Give the extent of all Plasmodium falciparum-infected red blood cells.
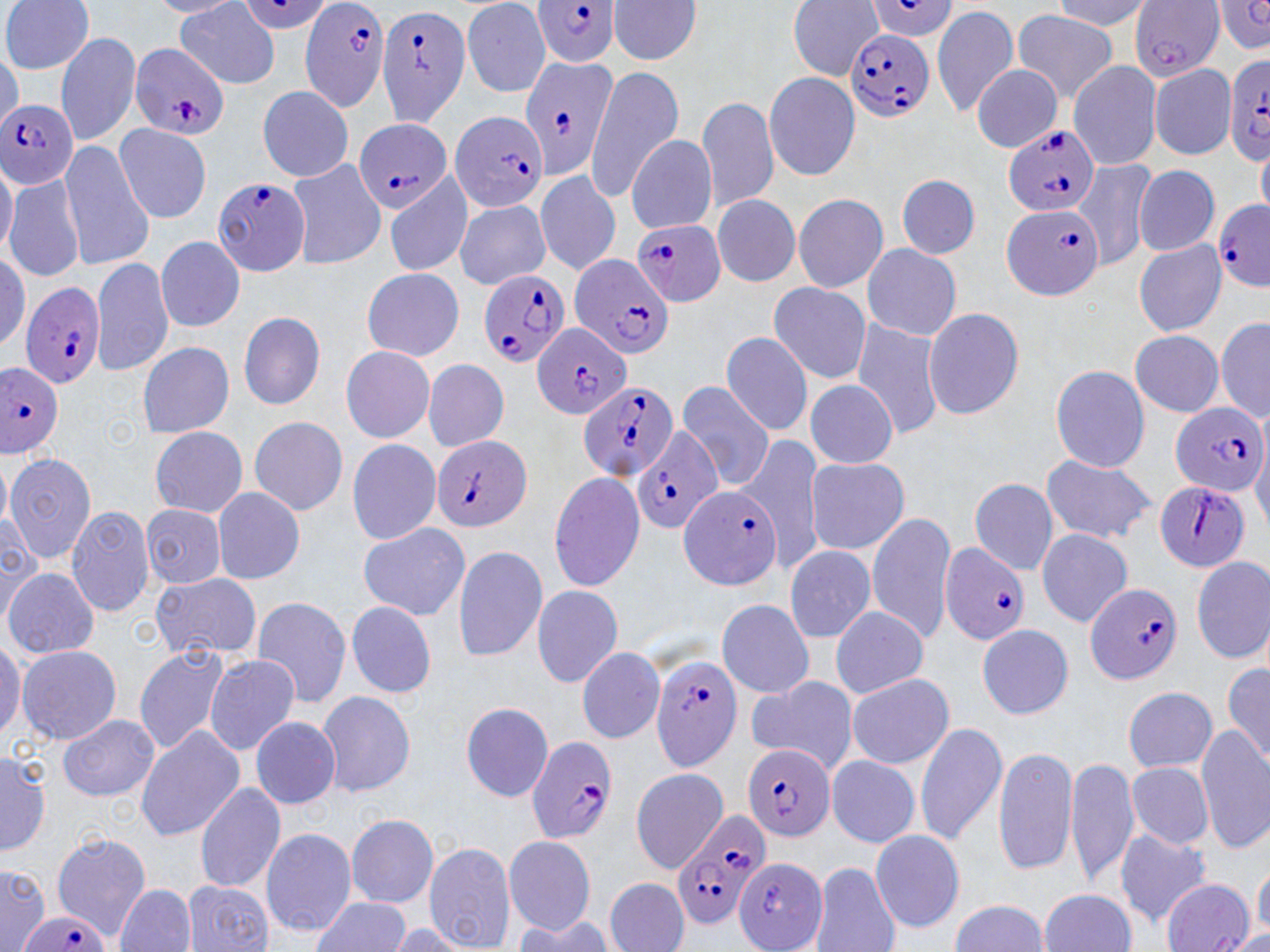

Approximate bounding boxes as named x1/y1/x2/y2 corners in pixels.
Plasmodium falciparum-infected red blood cells: (x1=533, y1=0, x2=622, y2=67), (x1=296, y1=5, x2=391, y2=110), (x1=380, y1=11, x2=466, y2=126), (x1=840, y1=26, x2=940, y2=122), (x1=134, y1=39, x2=226, y2=137), (x1=522, y1=55, x2=616, y2=182), (x1=1229, y1=56, x2=1270, y2=164), (x1=1, y1=99, x2=80, y2=191), (x1=350, y1=121, x2=454, y2=216), (x1=1006, y1=124, x2=1103, y2=213), (x1=211, y1=179, x2=307, y2=276), (x1=1209, y1=197, x2=1265, y2=293), (x1=1001, y1=202, x2=1101, y2=301), (x1=631, y1=220, x2=727, y2=307), (x1=567, y1=256, x2=673, y2=359), (x1=481, y1=271, x2=569, y2=373), (x1=21, y1=282, x2=103, y2=386), (x1=534, y1=324, x2=628, y2=419), (x1=0, y1=362, x2=64, y2=459), (x1=582, y1=388, x2=676, y2=478), (x1=1170, y1=401, x2=1268, y2=492), (x1=639, y1=429, x2=723, y2=538), (x1=428, y1=433, x2=532, y2=535), (x1=1150, y1=474, x2=1253, y2=570), (x1=680, y1=490, x2=780, y2=592), (x1=943, y1=541, x2=1024, y2=647), (x1=1083, y1=580, x2=1181, y2=684), (x1=644, y1=653, x2=745, y2=763), (x1=527, y1=738, x2=614, y2=838), (x1=744, y1=745, x2=833, y2=839), (x1=671, y1=808, x2=770, y2=928), (x1=16, y1=910, x2=112, y2=952).

Summary:
  - White blood cell locations: (x1=532, y1=575, x2=617, y2=690), (x1=989, y1=741, x2=1076, y2=877)
  - Uninfected red blood cell locations: (x1=3, y1=0, x2=91, y2=75), (x1=175, y1=0, x2=285, y2=87), (x1=610, y1=0, x2=699, y2=69), (x1=1129, y1=0, x2=1227, y2=79), (x1=790, y1=1, x2=860, y2=85), (x1=455, y1=2, x2=545, y2=98), (x1=935, y1=8, x2=1018, y2=119), (x1=1010, y1=8, x2=1121, y2=101), (x1=58, y1=36, x2=142, y2=144), (x1=1067, y1=59, x2=1163, y2=168), (x1=966, y1=63, x2=1048, y2=152), (x1=1150, y1=63, x2=1235, y2=161), (x1=766, y1=68, x2=855, y2=181), (x1=763, y1=69, x2=854, y2=183), (x1=591, y1=71, x2=683, y2=201), (x1=253, y1=91, x2=358, y2=179), (x1=698, y1=99, x2=787, y2=214), (x1=453, y1=106, x2=544, y2=208), (x1=112, y1=118, x2=208, y2=222), (x1=625, y1=133, x2=717, y2=235), (x1=62, y1=142, x2=153, y2=271), (x1=292, y1=158, x2=382, y2=272), (x1=1076, y1=161, x2=1150, y2=273), (x1=1128, y1=164, x2=1218, y2=256), (x1=530, y1=169, x2=620, y2=277), (x1=5, y1=173, x2=84, y2=277), (x1=898, y1=174, x2=978, y2=257), (x1=380, y1=188, x2=479, y2=278), (x1=707, y1=192, x2=797, y2=288), (x1=794, y1=192, x2=885, y2=290), (x1=453, y1=198, x2=551, y2=286), (x1=158, y1=236, x2=241, y2=333), (x1=1134, y1=240, x2=1228, y2=335), (x1=859, y1=243, x2=961, y2=343), (x1=92, y1=258, x2=170, y2=379), (x1=361, y1=267, x2=461, y2=361), (x1=767, y1=280, x2=870, y2=386), (x1=235, y1=311, x2=324, y2=413), (x1=923, y1=311, x2=1024, y2=421), (x1=848, y1=312, x2=946, y2=440), (x1=1218, y1=318, x2=1270, y2=419), (x1=1127, y1=329, x2=1225, y2=413), (x1=721, y1=333, x2=812, y2=435), (x1=134, y1=338, x2=231, y2=437), (x1=342, y1=349, x2=437, y2=445), (x1=420, y1=357, x2=504, y2=451), (x1=1048, y1=365, x2=1152, y2=474), (x1=674, y1=382, x2=778, y2=490), (x1=801, y1=384, x2=904, y2=470), (x1=247, y1=413, x2=344, y2=514), (x1=147, y1=426, x2=249, y2=518), (x1=347, y1=433, x2=439, y2=548), (x1=759, y1=436, x2=824, y2=575), (x1=7, y1=455, x2=96, y2=562), (x1=1044, y1=457, x2=1158, y2=539), (x1=796, y1=461, x2=908, y2=557), (x1=548, y1=478, x2=647, y2=589), (x1=972, y1=482, x2=1066, y2=577), (x1=214, y1=485, x2=302, y2=583), (x1=133, y1=502, x2=230, y2=590), (x1=69, y1=508, x2=156, y2=617), (x1=868, y1=514, x2=963, y2=646), (x1=354, y1=520, x2=468, y2=619), (x1=1038, y1=531, x2=1130, y2=628), (x1=786, y1=547, x2=881, y2=643), (x1=445, y1=550, x2=546, y2=657), (x1=1187, y1=552, x2=1270, y2=661), (x1=7, y1=567, x2=96, y2=660), (x1=147, y1=576, x2=262, y2=657), (x1=255, y1=599, x2=353, y2=703), (x1=346, y1=601, x2=434, y2=700), (x1=720, y1=604, x2=815, y2=697), (x1=825, y1=605, x2=927, y2=702), (x1=975, y1=617, x2=1070, y2=720), (x1=16, y1=646, x2=116, y2=742), (x1=135, y1=647, x2=235, y2=750), (x1=579, y1=649, x2=662, y2=741), (x1=205, y1=657, x2=305, y2=754), (x1=1222, y1=667, x2=1270, y2=759), (x1=848, y1=676, x2=954, y2=766), (x1=744, y1=677, x2=856, y2=774), (x1=1119, y1=680, x2=1213, y2=774), (x1=314, y1=693, x2=411, y2=798), (x1=456, y1=699, x2=549, y2=802), (x1=59, y1=717, x2=155, y2=799), (x1=245, y1=718, x2=339, y2=805), (x1=914, y1=726, x2=1007, y2=845), (x1=1196, y1=726, x2=1270, y2=849), (x1=136, y1=727, x2=242, y2=842), (x1=992, y1=749, x2=1077, y2=875), (x1=825, y1=758, x2=918, y2=848), (x1=1063, y1=758, x2=1138, y2=885), (x1=1125, y1=761, x2=1223, y2=851), (x1=635, y1=771, x2=724, y2=858), (x1=190, y1=784, x2=282, y2=892), (x1=340, y1=807, x2=434, y2=912), (x1=870, y1=826, x2=964, y2=932), (x1=1112, y1=828, x2=1213, y2=925), (x1=261, y1=830, x2=353, y2=933), (x1=54, y1=835, x2=148, y2=940), (x1=504, y1=839, x2=592, y2=935), (x1=427, y1=848, x2=514, y2=944), (x1=731, y1=859, x2=829, y2=950), (x1=812, y1=862, x2=897, y2=950), (x1=0, y1=874, x2=52, y2=952), (x1=604, y1=880, x2=685, y2=943), (x1=1161, y1=880, x2=1252, y2=952), (x1=186, y1=881, x2=269, y2=950), (x1=115, y1=883, x2=197, y2=952), (x1=1040, y1=888, x2=1135, y2=951), (x1=308, y1=896, x2=404, y2=950), (x1=947, y1=898, x2=1052, y2=952)
  - Slide-level diagnosis: Plasmodium falciparum
  - Field of view: single
  - Magnification: 1000x
  - Stain: May-Grünwald-Giemsa
  - Preparation: thin blood film
  - Image size: 1270×952 pixels
  - Modality: optical microscopy